Assess the morphology of the red blood cells.
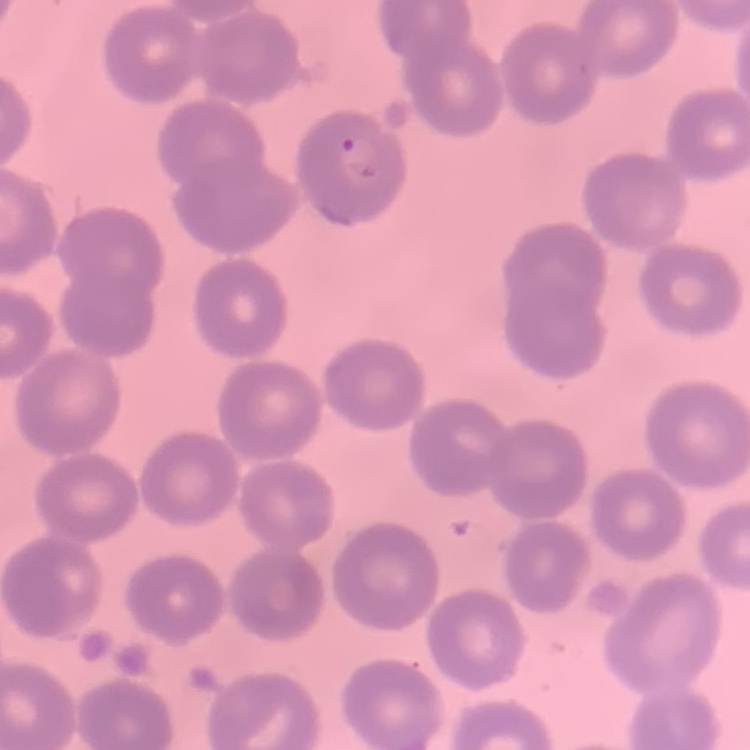

They show no rouleaux formation.

One tile cut from a larger photomicrograph. Thin blood film. Stained with either Field's or Giemsa.